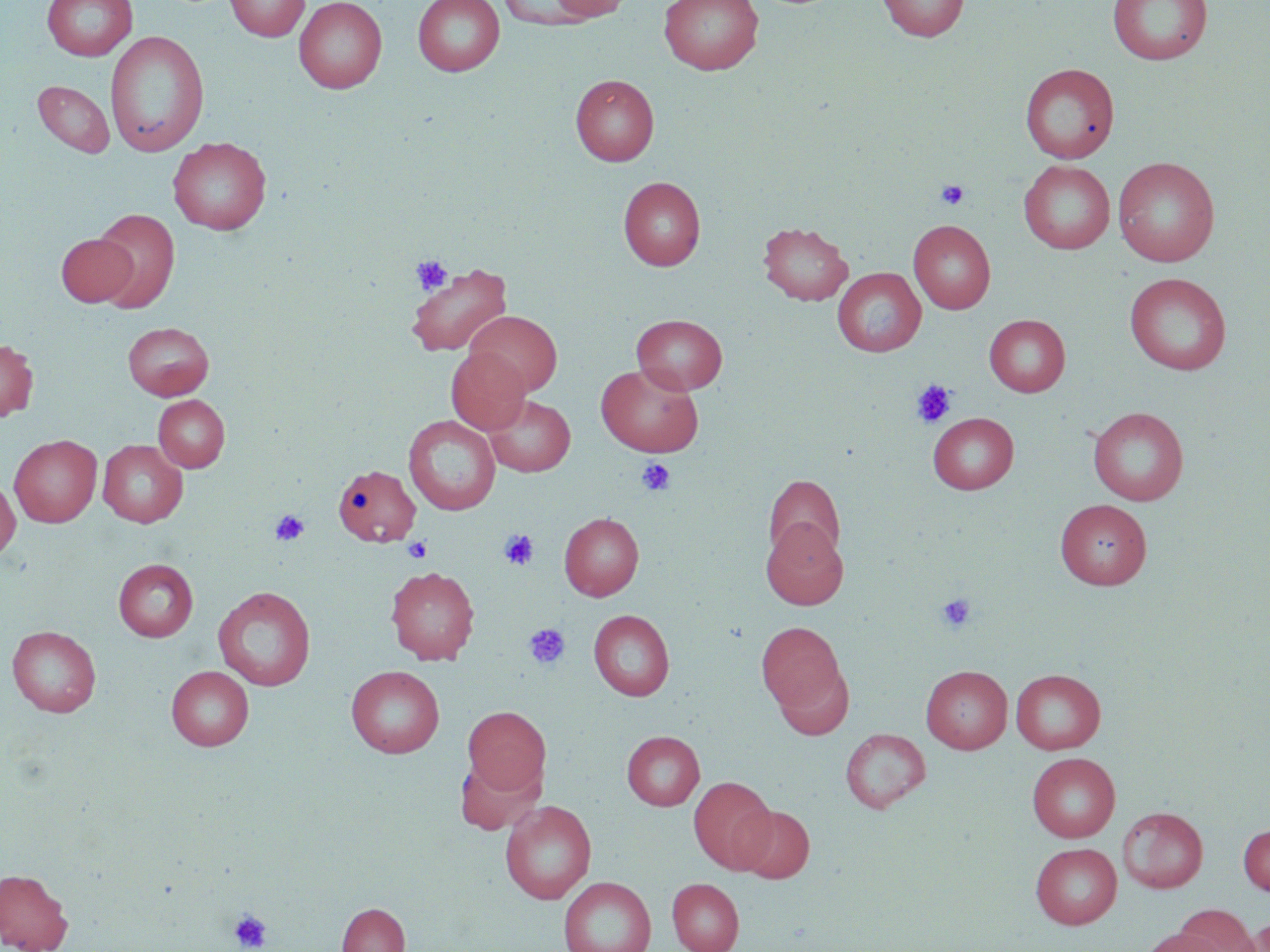
Summary:
  - Coordinate format: approximate bounding boxes as [x1, y1, x2, y2] in pixels
  - Uninfected red blood cell locations: [42, 0, 138, 61], [225, 0, 310, 41], [294, 0, 387, 93], [412, 0, 505, 76], [548, 0, 631, 21], [659, 0, 763, 75], [877, 0, 969, 42], [1107, 0, 1213, 65], [498, 1, 602, 29], [105, 30, 209, 156], [1020, 62, 1120, 163], [570, 74, 659, 166], [32, 80, 115, 157], [168, 137, 271, 235], [1113, 156, 1220, 267], [1019, 159, 1115, 254], [618, 177, 705, 271], [92, 208, 180, 312], [909, 219, 995, 314], [758, 221, 853, 305], [56, 233, 137, 307], [406, 263, 512, 357], [833, 267, 925, 356], [1124, 272, 1232, 375], [465, 310, 562, 397], [631, 314, 728, 394], [984, 314, 1070, 397], [123, 322, 214, 399], [0, 338, 38, 422], [446, 347, 531, 435], [596, 363, 704, 457], [153, 395, 230, 472], [485, 395, 575, 476], [1088, 407, 1190, 506], [928, 412, 1018, 494], [403, 414, 501, 516], [9, 435, 102, 527], [97, 440, 188, 527], [333, 464, 420, 547], [763, 474, 845, 564], [0, 477, 20, 560], [1055, 499, 1152, 589], [559, 512, 644, 600], [760, 517, 848, 610], [113, 558, 198, 641], [385, 566, 480, 665], [213, 586, 317, 691], [588, 609, 675, 700], [756, 621, 847, 718], [7, 625, 101, 717], [772, 659, 854, 741], [346, 665, 444, 757], [921, 665, 1013, 753], [166, 666, 254, 750], [1011, 669, 1105, 754], [463, 707, 550, 795], [840, 728, 931, 813], [622, 731, 704, 810], [1027, 752, 1120, 842], [454, 753, 546, 835], [689, 776, 777, 874], [500, 800, 597, 904], [736, 805, 815, 884], [1117, 806, 1208, 892], [1238, 823, 1270, 896], [1030, 842, 1122, 929], [0, 869, 73, 952], [559, 876, 656, 952], [667, 878, 744, 952], [336, 902, 410, 952], [1171, 905, 1262, 952], [1245, 917, 1270, 952], [1139, 928, 1229, 952]
  - Platelet locations: [936, 179, 969, 210], [411, 255, 453, 294], [911, 380, 955, 428], [637, 457, 676, 497], [270, 509, 309, 547], [499, 529, 538, 570], [403, 536, 433, 563], [936, 592, 977, 632], [523, 623, 571, 669], [229, 909, 272, 951]
  - Slide-level diagnosis: no evidence of blood parasites
  - Preparation: thin blood smear
  - Stain: May-Grünwald-Giemsa
  - Image size: 1270×952 pixels
  - Magnification: 1000x
  - Modality: light microscopy
  - Field of view: single